Outline platelets.
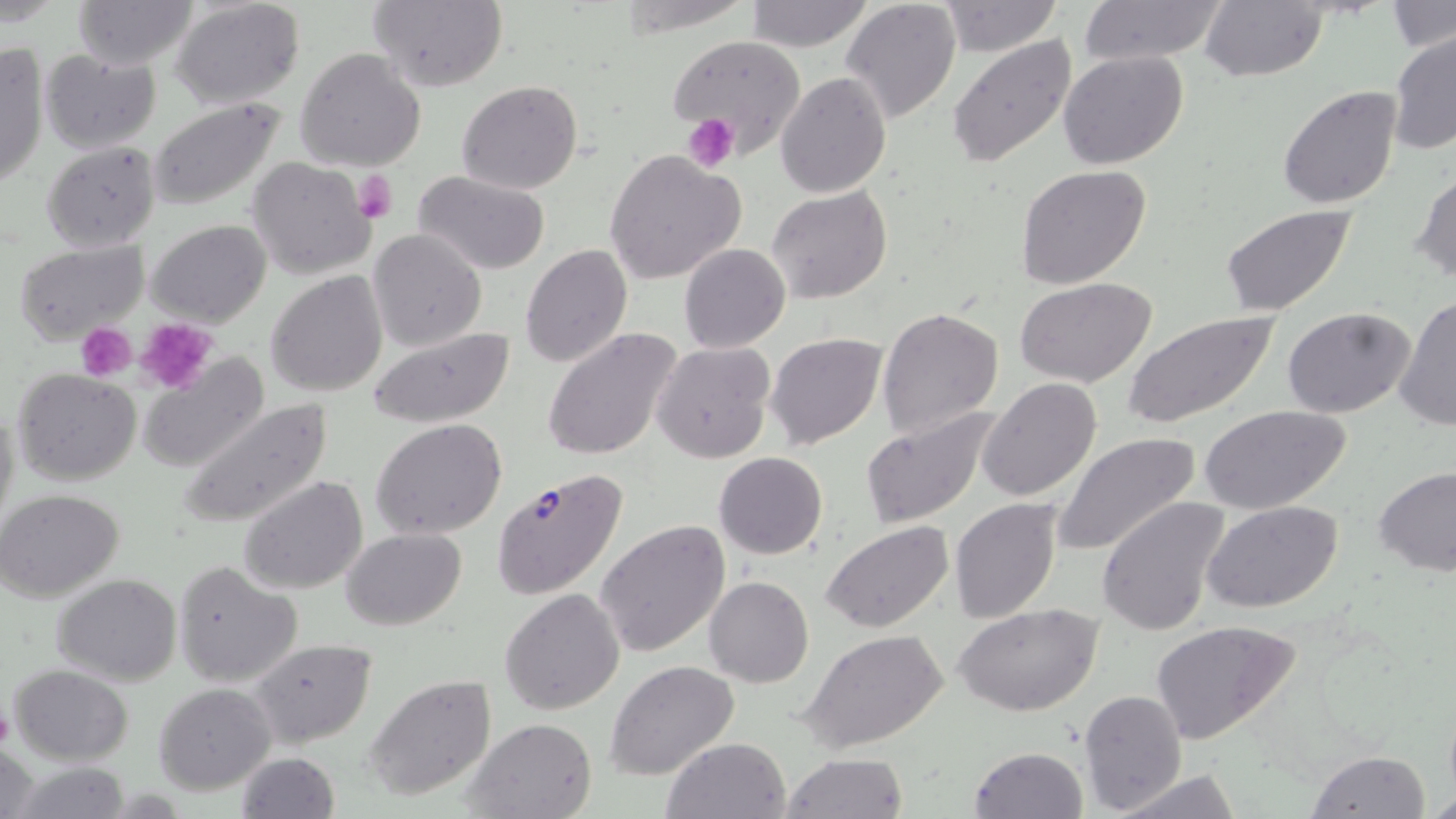
Approximate bounding boxes as (x1,y1)-(x2,y2) corner pairs in pixels.
Platelets: (683,114)-(739,169), (351,169)-(399,225), (133,318)-(216,394), (78,322)-(136,381), (0,701)-(15,753).

Uninfected red blood cell locations: (74,0)-(194,70), (172,0)-(304,109), (616,0)-(749,32), (745,0)-(873,51), (840,0)-(962,123), (1081,0)-(1225,68), (1199,0)-(1327,82), (369,1)-(507,90), (937,1)-(1064,56), (1389,1)-(1453,54), (1388,32)-(1456,156), (668,34)-(807,159), (948,36)-(1077,170), (0,42)-(50,193), (295,47)-(427,172), (42,51)-(162,154), (1058,51)-(1188,170), (776,71)-(891,196), (457,80)-(583,195), (1278,85)-(1402,209), (148,99)-(287,210), (43,142)-(161,252), (606,149)-(747,285), (248,157)-(379,280), (1014,164)-(1152,289), (1410,170)-(1456,286), (415,171)-(552,274), (766,185)-(893,304), (1218,204)-(1359,318), (146,219)-(271,327), (367,229)-(486,351), (14,239)-(149,343), (679,243)-(790,353), (520,245)-(633,367), (265,269)-(387,396), (1013,276)-(1158,387), (1393,296)-(1456,431), (877,305)-(1004,439), (1283,307)-(1417,419), (1122,309)-(1281,428), (369,326)-(517,428), (543,328)-(684,463), (766,333)-(887,448), (652,341)-(777,464), (139,357)-(267,474), (13,369)-(141,486), (978,376)-(1103,502), (177,398)-(333,528), (0,402)-(20,530), (1197,402)-(1354,514), (861,407)-(1000,528), (370,418)-(508,540), (1053,430)-(1204,561), (715,452)-(827,559), (1374,469)-(1456,577), (238,475)-(369,593), (0,489)-(126,603), (1097,497)-(1230,635), (949,498)-(1063,623), (1202,501)-(1345,613), (596,517)-(731,657), (821,521)-(954,635), (342,528)-(467,631), (172,561)-(303,688), (52,573)-(183,685), (704,576)-(814,688), (500,588)-(623,714), (955,602)-(1104,716), (1148,620)-(1301,745), (800,629)-(949,756), (248,639)-(378,749), (605,660)-(739,780), (8,664)-(134,766), (363,674)-(496,802), (153,685)-(274,795), (1079,688)-(1186,815), (465,718)-(596,819), (661,736)-(792,819), (0,742)-(42,819), (969,746)-(1088,819), (1306,750)-(1432,818), (234,752)-(339,819), (781,753)-(909,818), (10,764)-(136,819), (1110,770)-(1243,819), (1427,788)-(1456,816). Plasmodium falciparum-infected red blood cell locations: (488,466)-(631,602). Slide-level diagnosis: Plasmodium falciparum. Thin blood smear. Single field of view. Image is 1456×819 pixels. May-Grünwald-Giemsa stain. Optical microscopy. 1000x magnification.